Name the cell type shown.
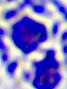

This is a leukocyte.

{
  "magnification": "400x",
  "modality": "micrograph"
}